Locate and identify every blood parasite.
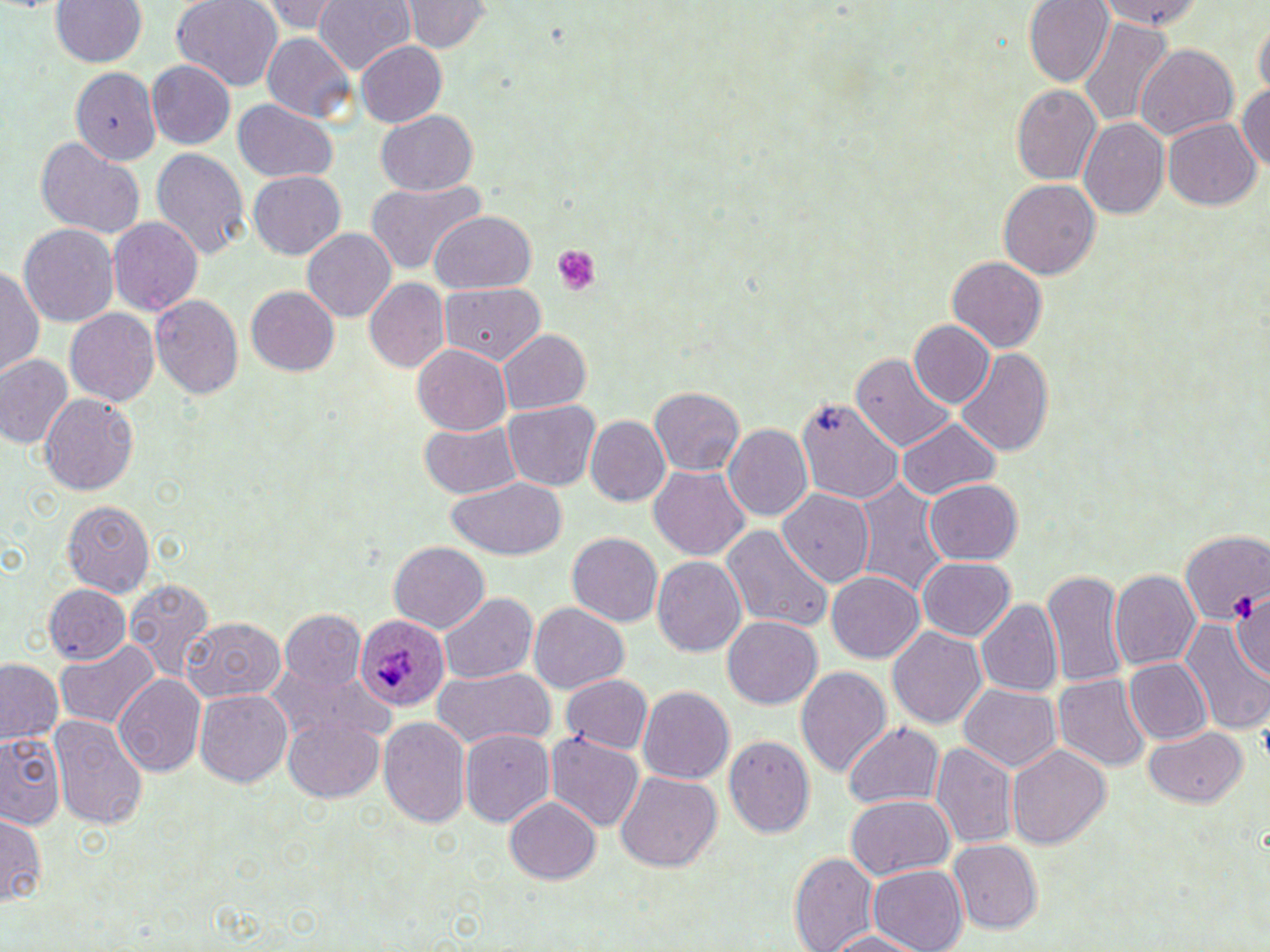

Approximate bounding boxes as (x1,y1)-(x2,y2) corner pairs in pixels.
Plasmodium ovale-infected red blood cells: (354,615)-(451,712).
No Plasmodium falciparum, Plasmodium malariae, Plasmodium vivax, Babesia divergens, or Trypanosoma brucei observed.

Uninfected red blood cell locations: (49,0)-(148,68), (169,0)-(284,91), (255,0)-(348,35), (313,0)-(417,73), (1099,0)-(1204,28), (1023,1)-(1113,86), (400,2)-(493,51), (1252,15)-(1269,97), (1078,18)-(1174,127), (260,32)-(355,122), (355,40)-(447,127), (1136,45)-(1237,139), (147,60)-(236,149), (70,66)-(161,166), (1234,85)-(1268,170), (1011,86)-(1101,184), (1025,98)-(1157,203), (232,99)-(338,183), (376,109)-(476,196), (1079,118)-(1168,218), (1162,120)-(1260,209), (33,137)-(144,238), (150,147)-(251,259), (247,170)-(346,258), (364,178)-(485,275), (997,179)-(1100,279), (429,211)-(537,294), (107,216)-(202,316), (18,223)-(119,328), (302,227)-(397,322), (946,256)-(1048,351), (0,264)-(43,377), (364,279)-(449,373), (438,281)-(545,363), (245,285)-(339,376), (148,293)-(243,397), (64,308)-(160,405), (910,320)-(995,408), (499,329)-(591,414), (412,344)-(512,436), (958,347)-(1052,458), (852,352)-(956,452), (0,353)-(74,449), (650,386)-(743,476), (40,392)-(138,497), (797,397)-(903,504), (503,400)-(599,491), (585,416)-(670,505), (895,418)-(1001,498), (419,419)-(524,500), (723,423)-(813,521), (649,466)-(750,561), (446,475)-(569,560), (855,478)-(949,596), (925,479)-(1022,564), (778,489)-(874,586), (61,499)-(155,597), (721,525)-(832,635), (1178,529)-(1269,623), (566,532)-(662,625), (389,541)-(488,631), (652,556)-(748,656), (917,557)-(1016,640), (1042,569)-(1129,687), (1109,569)-(1201,670), (827,571)-(923,662), (125,577)-(217,682), (1139,579)-(1252,717), (43,584)-(130,665), (1229,587)-(1270,678), (438,592)-(537,682), (976,599)-(1064,695), (529,601)-(629,693), (280,609)-(367,689), (182,616)-(286,702), (722,616)-(822,708), (1181,618)-(1270,735), (887,627)-(988,728), (55,639)-(159,728), (1126,659)-(1211,743), (0,660)-(65,746), (270,664)-(393,747), (797,666)-(892,778), (433,667)-(553,749), (115,674)-(207,777), (561,674)-(652,753), (1053,675)-(1151,770), (958,683)-(1060,772), (638,685)-(735,784), (195,689)-(293,787), (49,714)-(146,829), (282,716)-(385,803), (378,716)-(470,826), (841,721)-(945,809), (459,728)-(555,826), (1143,728)-(1247,807), (0,729)-(65,832), (546,733)-(643,830), (723,734)-(815,838), (932,742)-(1019,850), (1007,746)-(1110,849), (614,771)-(721,872), (846,794)-(954,880), (504,795)-(601,882), (0,812)-(45,908), (948,839)-(1042,932), (789,851)-(881,952), (867,865)-(968,952), (819,930)-(924,951). Platelet locations: (549,245)-(602,296), (1231,595)-(1259,621). Slide-level diagnosis: Plasmodium ovale. Thin blood film. May-Grünwald-Giemsa-stained preparation. Captured at 1000x magnification. Light microscopy. Image is 1270×952 pixels. Single field of view.